Give the position of every malaria parasite and every leukocyte.
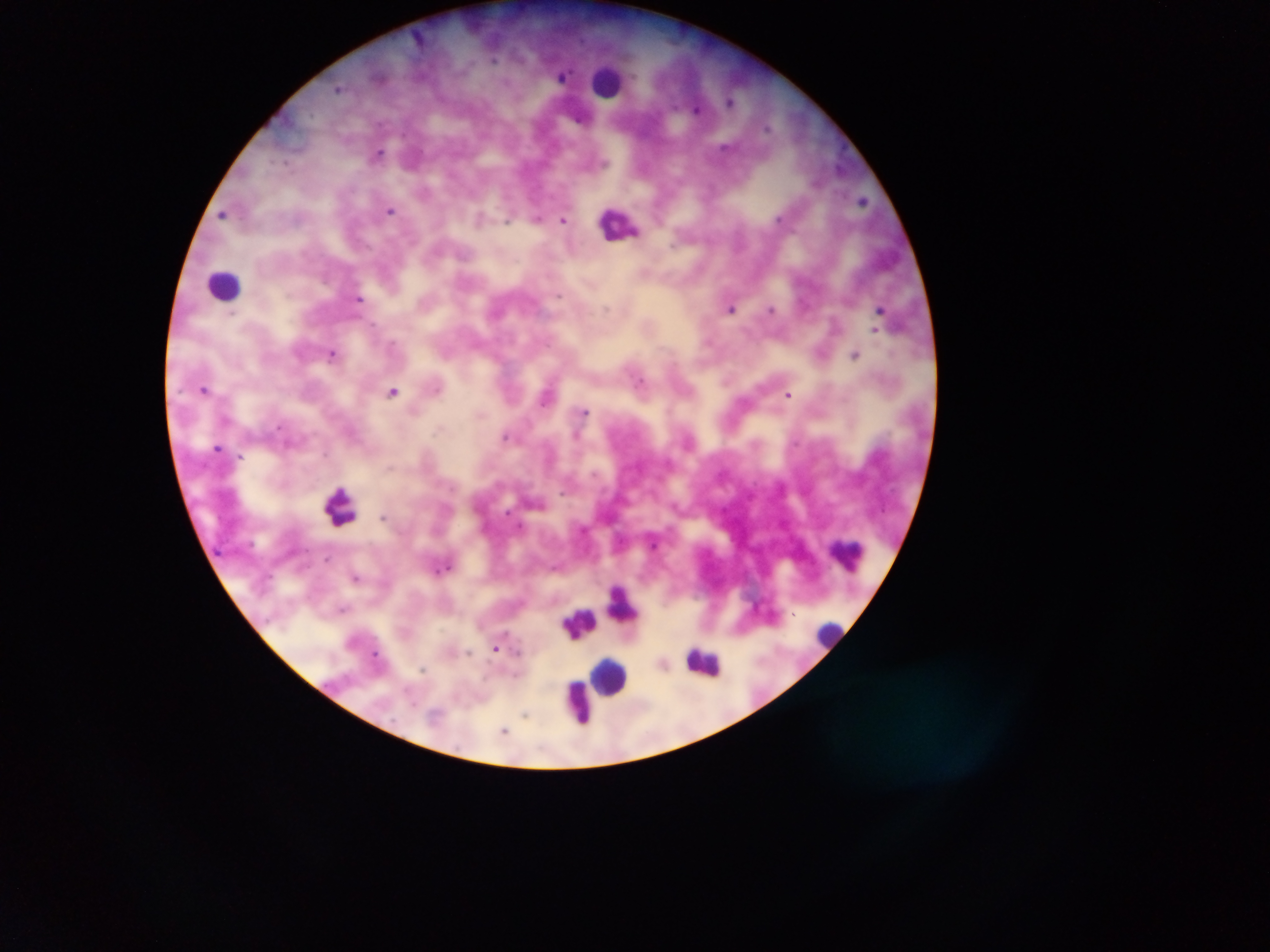

Approximate centers as (x, y) in pixels.
Malaria parasites: (494, 60), (564, 76), (338, 88), (731, 101), (697, 109), (379, 153), (864, 200), (390, 210), (222, 215), (537, 218), (563, 220), (507, 221), (672, 246), (559, 296), (359, 298), (606, 308), (731, 308), (771, 309), (232, 315), (374, 324), (874, 331), (392, 344), (332, 353), (855, 354), (641, 381), (204, 389), (392, 392), (788, 394), (545, 397), (585, 411), (277, 427), (437, 429), (577, 436), (506, 437), (218, 447), (325, 454), (241, 456), (594, 473), (562, 492), (382, 517), (653, 543), (328, 557), (555, 567), (356, 578), (343, 609), (495, 647), (469, 652), (376, 654), (422, 669), (525, 714), (437, 716), (504, 730).
Leukocytes: (608, 81), (620, 223), (225, 283), (340, 507), (849, 556), (623, 604), (579, 623), (828, 631), (703, 663), (610, 675), (578, 702).

Summary:
  - Field of view: single
  - Preparation: thick blood film
  - Image size: 1270×952 pixels
  - Country: Ghana
  - Capture: mobile-phone photograph through a microscope